Assess this cell for malaria.
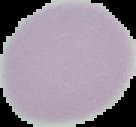

It is uninfected.

Summary:
  - Image type: segmented cell region on a black background
  - Image size: 136×127 pixels
  - Preparation: thin blood smear